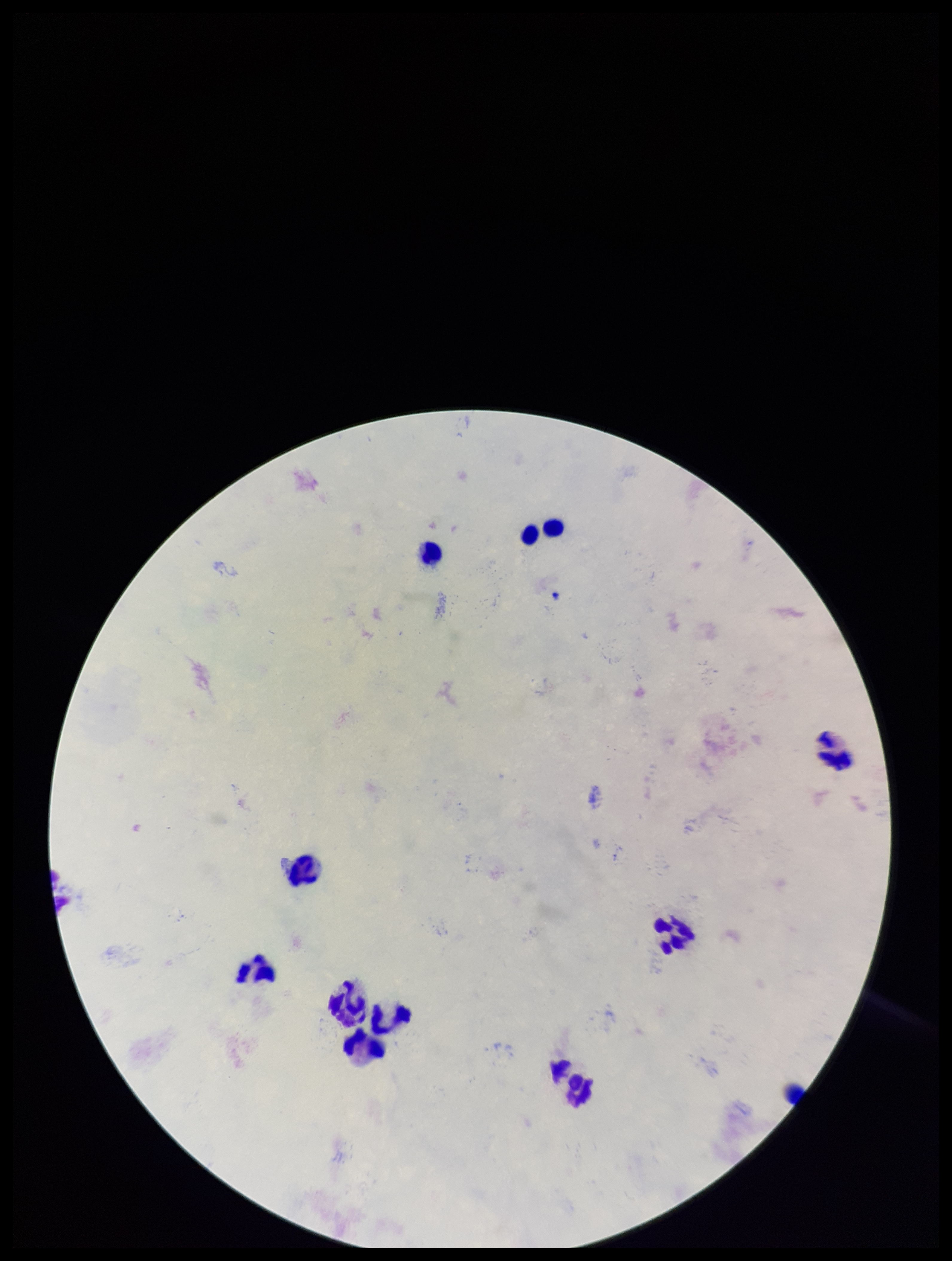

field_of_view: single
parasite_count: 0
preparation: thick blood smear
stain: Giemsa
image_size: 952×1261 pixels
capture: smartphone photograph through the microscope eyepiece
patient_malaria_status: negative
plasmodium_parasites: none seen
leukocyte_count: 11